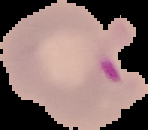

The area outside the segmented cell region is set to black. From a thin blood smear. Image is 148×130 pixels. Malaria status: parasitized.